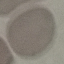

Summary:
  - Result: no malaria parasites seen
  - Preparation: thin smear
  - Stain: Giemsa
  - Image type: automatically extracted cell patch, resized to 64 × 64 pixels
  - Capture: smartphone camera at the microscope eyepiece